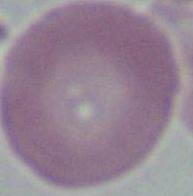
Summary:
  - Modality: photomicrograph
  - Identification: erythrocyte
  - Magnification: 1000x